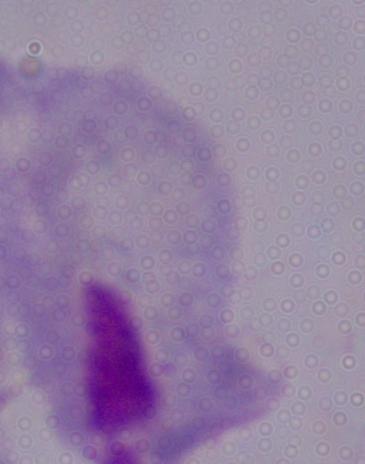

magnification = 1000x
modality = micrograph
identification = trichomonad